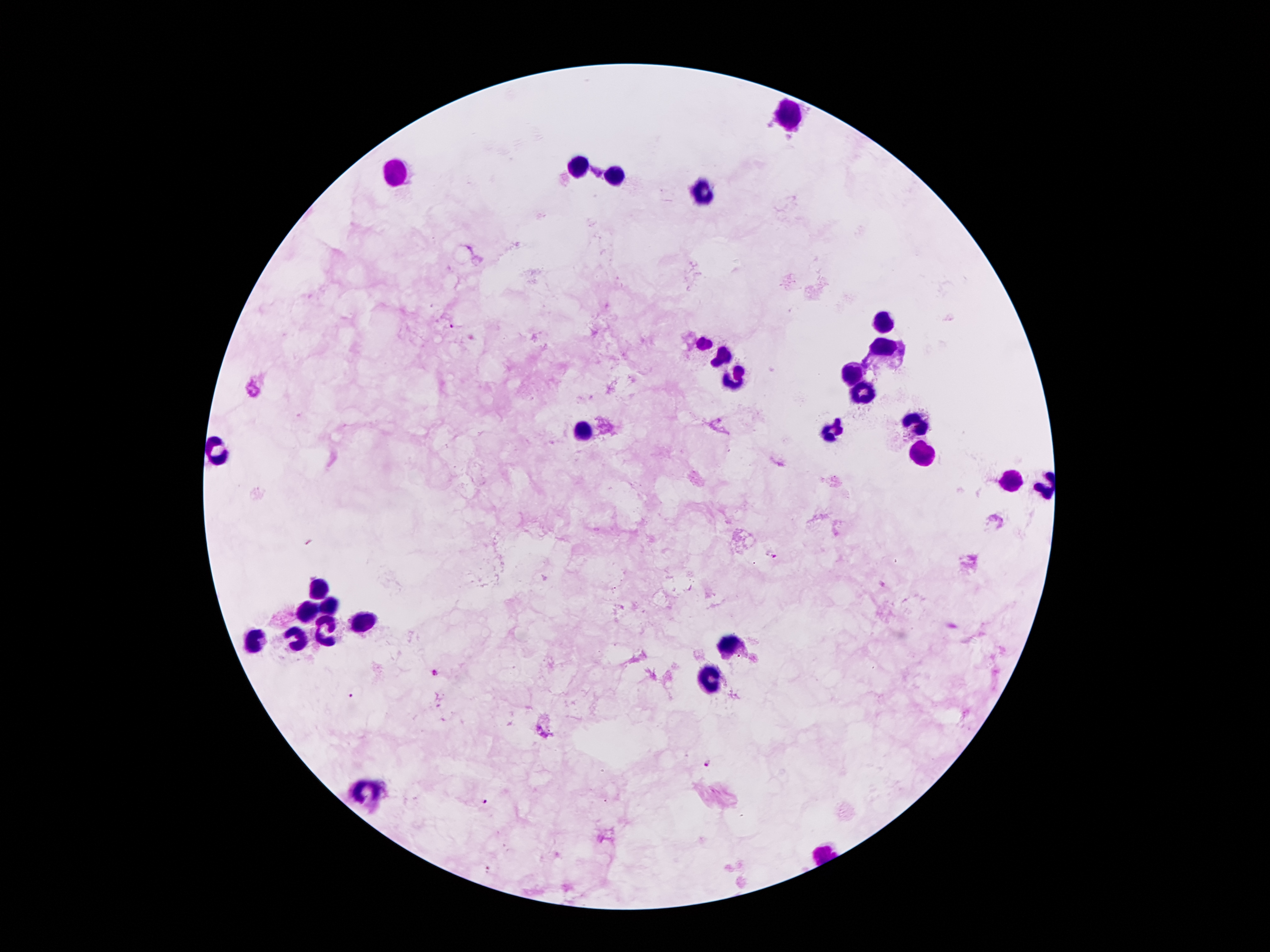

Approximate centers as {x, y} in pixels.
Summary:
  - Leukocyte locations: {786, 113}, {579, 162}, {399, 175}, {616, 175}, {702, 192}, {885, 321}, {702, 340}, {885, 351}, {720, 353}, {853, 368}, {732, 379}, {863, 392}, {915, 421}, {831, 426}, {584, 432}, {213, 446}, {922, 454}, {1011, 478}, {312, 589}, {327, 604}, {305, 612}, {359, 620}, {327, 629}, {255, 639}, {727, 639}, {295, 641}, {712, 681}, {369, 784}
  - Plasmodium parasite locations: {453, 325}, {310, 543}, {772, 555}, {435, 672}, {352, 697}, {542, 732}, {707, 763}, {486, 801}, {488, 867}
  - Capture: smartphone camera through the microscope eyepiece
  - Image size: 1270×952 pixels
  - Field of view: single
  - Stain: Giemsa
  - Magnification: 100x
  - Preparation: thick blood film
  - Patient malaria status: positive for Plasmodium falciparum